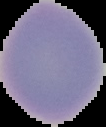
Image is 106×127 pixels. From a thin blood film. Malaria status: uninfected. Cell region segmented out of the field of view; the surrounding area is masked to black.